Comment on the morphology of the erythrocytes.
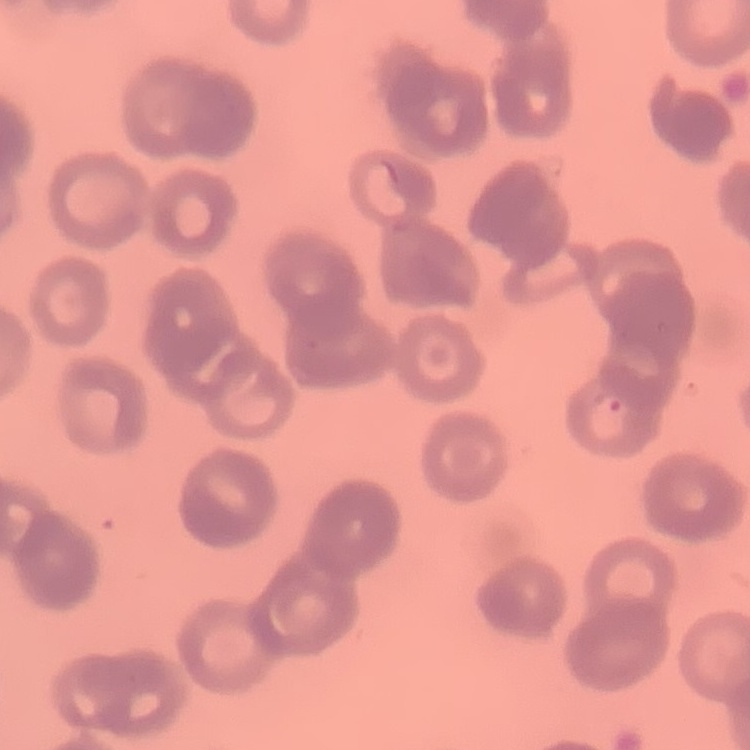
Rouleaux formation.

One tile cut from a larger photomicrograph. Thin blood smear. Field's or Giemsa stain.